Assess this cell for malaria.
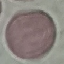

It is uninfected.

Cell patch, automatically extracted from a larger field of view and resized to 64 × 64 pixels. Acquired by smartphone through the microscope eyepiece. Giemsa-stained preparation. Thin smear of blood.